Outline each Plasmodium ovale-infected red blood cell.
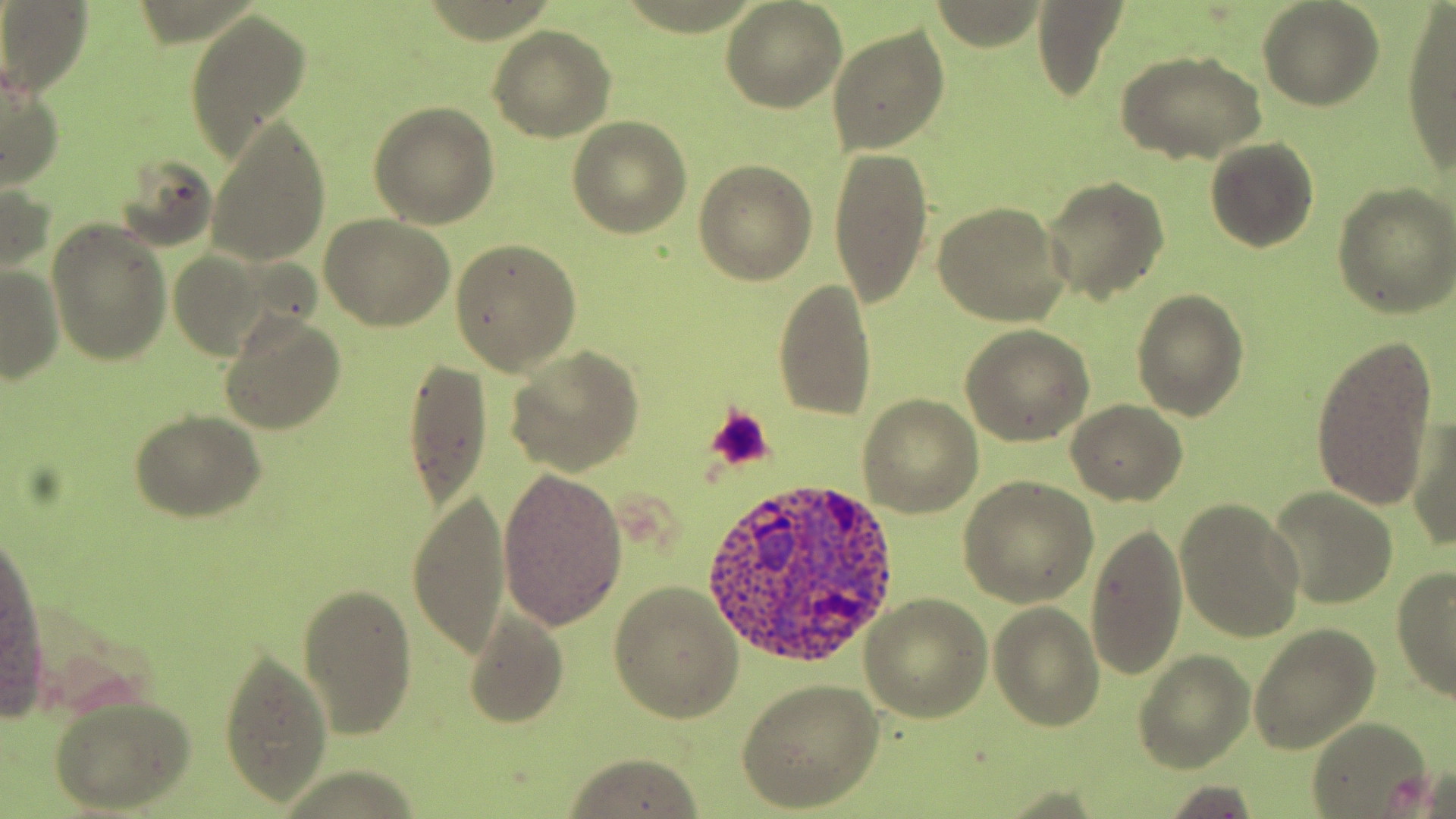

Approximate bounding boxes as (x1,y1)-(x2,y2) corner pairs in pixels.
Plasmodium ovale-infected red blood cells: (700,483)-(898,670).

slide-level diagnosis = Plasmodium ovale
image size = 1456×819 pixels
magnification = 1000x
uninfected red blood cell locations = approximate bounding boxes as (x1,y1)-(x2,y2) corner pairs in pixels: (0,1)-(92,99), (722,2)-(847,111), (1029,2)-(1130,102), (1257,2)-(1383,110), (1400,6)-(1456,172), (185,7)-(313,168), (826,25)-(950,155), (489,27)-(616,142), (1117,49)-(1266,165), (1,65)-(66,192), (368,102)-(499,229), (206,117)-(331,268), (567,118)-(692,239), (1206,138)-(1318,253), (827,145)-(934,309), (116,153)-(219,254), (693,160)-(817,284), (2,175)-(55,287), (1043,177)-(1169,301), (1332,184)-(1456,319), (932,200)-(1070,326), (321,215)-(455,331), (45,218)-(174,366), (451,239)-(583,377), (166,249)-(273,362), (1,260)-(64,384), (775,278)-(878,419), (1132,288)-(1249,420), (219,312)-(347,434), (961,327)-(1093,444), (1310,334)-(1440,514), (504,345)-(644,475), (402,355)-(491,515), (857,393)-(984,516), (1066,399)-(1187,505), (129,411)-(265,522), (1406,413)-(1456,553), (497,468)-(627,631), (959,477)-(1097,607), (1268,487)-(1399,607), (406,489)-(511,658), (1174,497)-(1306,644), (1085,519)-(1187,682), (1,539)-(48,702), (1391,564)-(1456,704), (609,581)-(745,722), (295,582)-(418,740), (860,593)-(991,722), (989,602)-(1103,732), (463,608)-(570,727), (1248,622)-(1381,754), (220,649)-(335,805), (1135,651)-(1252,770), (737,678)-(884,812), (49,696)-(193,809), (1304,718)-(1431,815), (564,753)-(705,817)
stain = May-Grünwald-Giemsa
field of view = one of a larger specimen
platelet locations = approximate bounding boxes as (x1,y1)-(x2,y2) corner pairs in pixels: (705,407)-(772,471)
modality = light microscopy
preparation = thin blood film